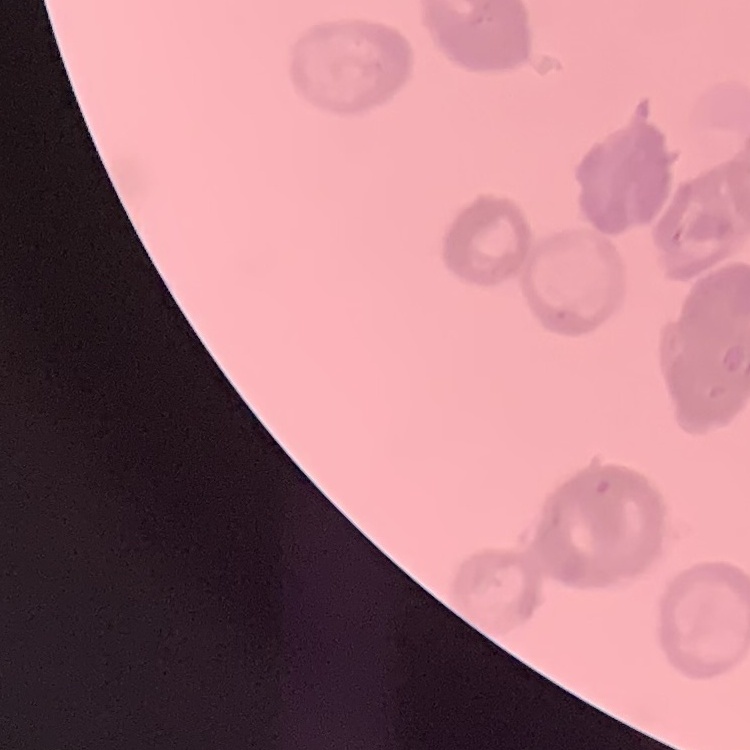

Summary:
  - Red blood cell morphology: rouleaux formation
  - Preparation: thin blood film
  - Stain: Field's or Giemsa
  - Image type: square crop of a larger photomicrograph